Identify the parasite.
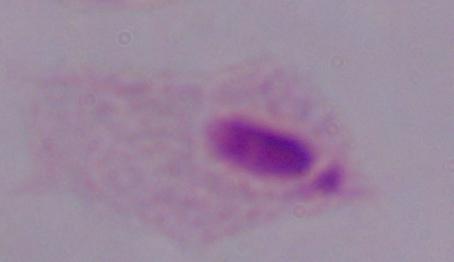
A trichomonad.

1000x magnification. Photomicrograph.